Assess this cell for malaria.
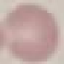

It is uninfected.

{
  "capture": "smartphone camera at the microscope eyepiece",
  "image_type": "cell patch, automatically extracted from a larger field of view and resized to 64 × 64 pixels",
  "preparation": "thin smear",
  "stain": "Giemsa"
}